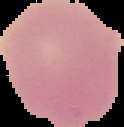

preparation: thin blood film
result: no Plasmodium parasites seen
image_size: 124×127 pixels
image_type: segmented cell region with the area outside set to black